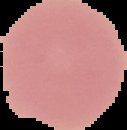

image_size: 127×130 pixels
result: negative for malaria parasites
image_type: cell region segmented out of the field of view; surrounding area masked to black
preparation: thin blood film